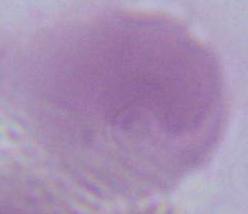

magnification = 1000x
modality = micrograph
identification = red blood cell